Assess this cell for malaria.
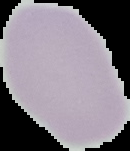

Uninfected.

image type = segmented cell region on a black background
image size = 130×151 pixels
preparation = thin blood smear